Locate every uninfected red blood cell.
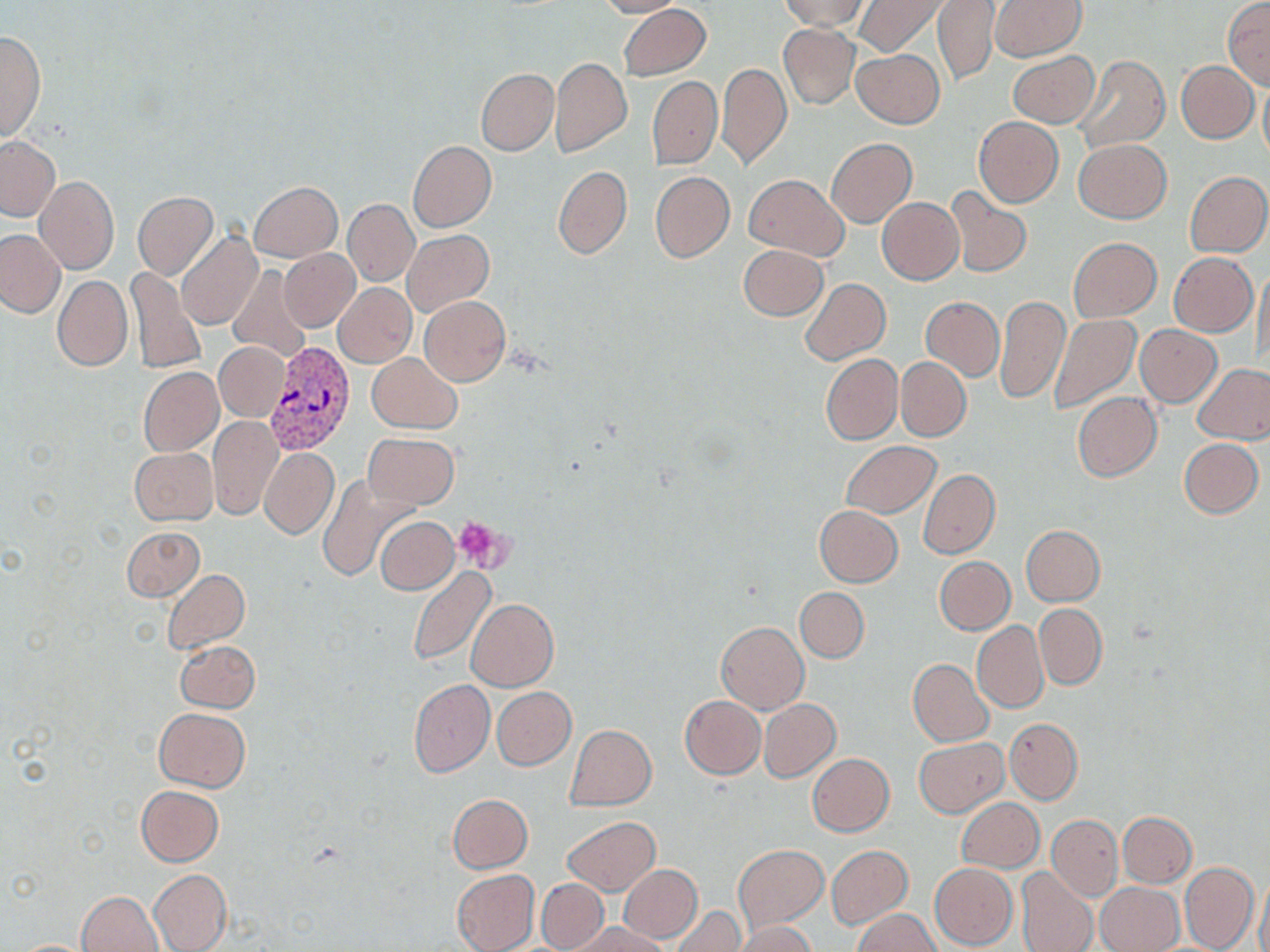
Approximate bounding boxes as [x1, y1, x2, y2] in pixels.
Uninfected red blood cells: [596, 0, 685, 19], [779, 0, 868, 30], [854, 0, 946, 57], [934, 0, 999, 86], [991, 1, 1086, 62], [1223, 1, 1270, 88], [618, 4, 710, 81], [778, 24, 860, 109], [0, 31, 45, 143], [852, 49, 943, 128], [1007, 51, 1098, 128], [1072, 54, 1170, 154], [551, 57, 632, 157], [1176, 60, 1259, 143], [717, 63, 791, 168], [476, 68, 559, 156], [647, 76, 721, 168], [1259, 76, 1270, 165], [973, 116, 1063, 208], [0, 134, 59, 222], [826, 138, 915, 228], [1074, 139, 1171, 222], [408, 141, 496, 231], [552, 165, 632, 259], [1185, 170, 1269, 257], [650, 171, 734, 262], [743, 174, 848, 261], [35, 175, 118, 274], [248, 181, 342, 262], [945, 185, 1032, 279], [133, 192, 218, 279], [877, 197, 964, 285], [344, 198, 419, 286], [0, 228, 65, 318], [403, 229, 493, 316], [176, 231, 263, 332], [1068, 237, 1162, 323], [739, 245, 827, 320], [278, 247, 360, 332], [1170, 251, 1256, 337], [228, 264, 314, 363], [1253, 264, 1269, 372], [126, 266, 207, 373], [51, 274, 132, 372], [800, 278, 890, 365], [333, 283, 416, 368], [921, 295, 1004, 380], [995, 295, 1070, 405], [420, 296, 510, 386], [1049, 315, 1142, 415], [1135, 325, 1222, 406], [215, 342, 288, 421], [368, 353, 462, 433], [821, 354, 902, 444], [896, 358, 971, 441], [1193, 363, 1270, 444], [138, 367, 224, 456], [1072, 392, 1161, 481], [209, 416, 283, 520], [137, 432, 279, 522], [362, 434, 459, 510], [1179, 437, 1264, 518], [841, 441, 940, 518], [130, 447, 218, 525], [260, 448, 338, 539], [918, 468, 1000, 559], [317, 474, 417, 582], [814, 504, 904, 587], [375, 517, 458, 594], [1021, 525, 1106, 606], [121, 527, 204, 601], [934, 557, 1015, 634], [407, 566, 498, 667], [163, 568, 250, 654], [796, 587, 868, 662], [466, 599, 558, 691], [1035, 604, 1107, 689], [972, 621, 1047, 712], [715, 622, 808, 714], [175, 639, 260, 713], [909, 659, 994, 747], [408, 678, 495, 777], [491, 687, 576, 770], [679, 695, 766, 779], [758, 698, 841, 781], [154, 707, 250, 791], [1005, 719, 1083, 803], [565, 723, 656, 811], [913, 738, 1008, 817], [807, 753, 895, 836], [135, 786, 223, 866], [448, 795, 532, 873], [957, 797, 1044, 873], [1118, 811, 1197, 887], [1047, 815, 1123, 899], [562, 816, 660, 895], [734, 845, 828, 931], [827, 846, 911, 928], [1179, 862, 1258, 952], [930, 863, 1017, 950], [618, 864, 703, 943], [149, 868, 232, 952], [1016, 868, 1098, 952], [451, 869, 539, 952], [1257, 869, 1270, 952], [536, 878, 609, 951], [1094, 882, 1183, 952], [75, 891, 164, 952], [671, 906, 744, 952], [853, 909, 940, 952], [568, 921, 670, 952], [736, 922, 816, 952], [9, 939, 104, 951].

slide-level diagnosis = Plasmodium vivax
preparation = thin blood smear
image size = 1270×952 pixels
field of view = single
modality = optical microscopy
Plasmodium vivax-infected red blood cell locations = approximate bounding boxes as [x1, y1, x2, y2] in pixels: [264, 342, 356, 457]
platelet locations = approximate bounding boxes as [x1, y1, x2, y2] in pixels: [452, 517, 514, 573]
magnification = 1000x
stain = May-Grünwald-Giemsa